Report the malaria status of this cell.
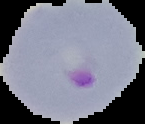

It is parasitized.

From a thin blood film. Cell region segmented out of the field of view; the surrounding area is masked to black. Image is 145×124 pixels.